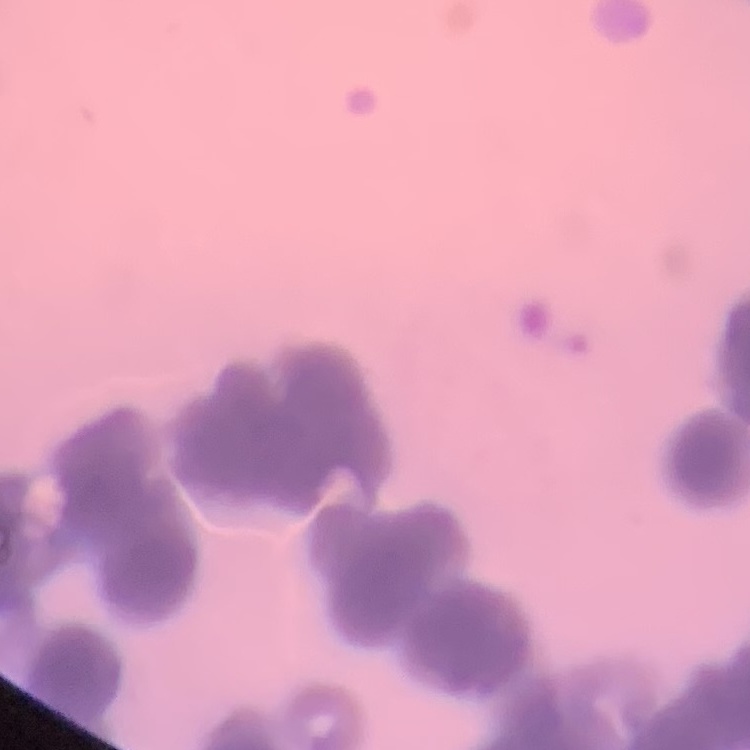 The erythrocytes show rouleaux formation. Stained with either Field's or Giemsa. Square crop of a larger photomicrograph. Thin peripheral smear.